Assess this cell for malaria.
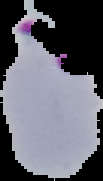

Parasitized.

Cell region segmented out of the field of view; the surrounding area is masked to black. From a thin blood smear. Image is 103×181 pixels.